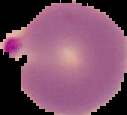
Summary:
  - Image size: 127×115 pixels
  - Image type: segmented cell region with the area outside set to black
  - Preparation: thin blood smear
  - Result: Plasmodium parasites detected